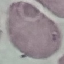
Summary:
  - Malaria status: uninfected
  - Image type: automatically extracted cell patch, resized to 64 × 64 pixels
  - Capture: smartphone camera at the microscope eyepiece
  - Preparation: thin blood film
  - Stain: Giemsa